Name the parasite shown.
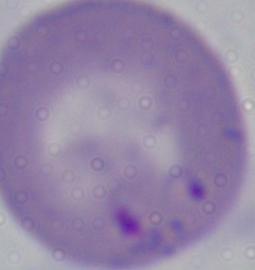
This is Babesia.

Summary:
  - Modality: photomicrograph
  - Magnification: 1000x